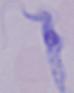

modality = micrograph
magnification = 1000x
identification = trypanosome